Assess this cell for malaria.
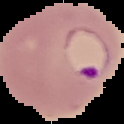

It is parasitized.

Image is 124×124 pixels. The area outside the segmented cell region is set to black. From a thin blood film.